Locate every blood parasite and identify its species.
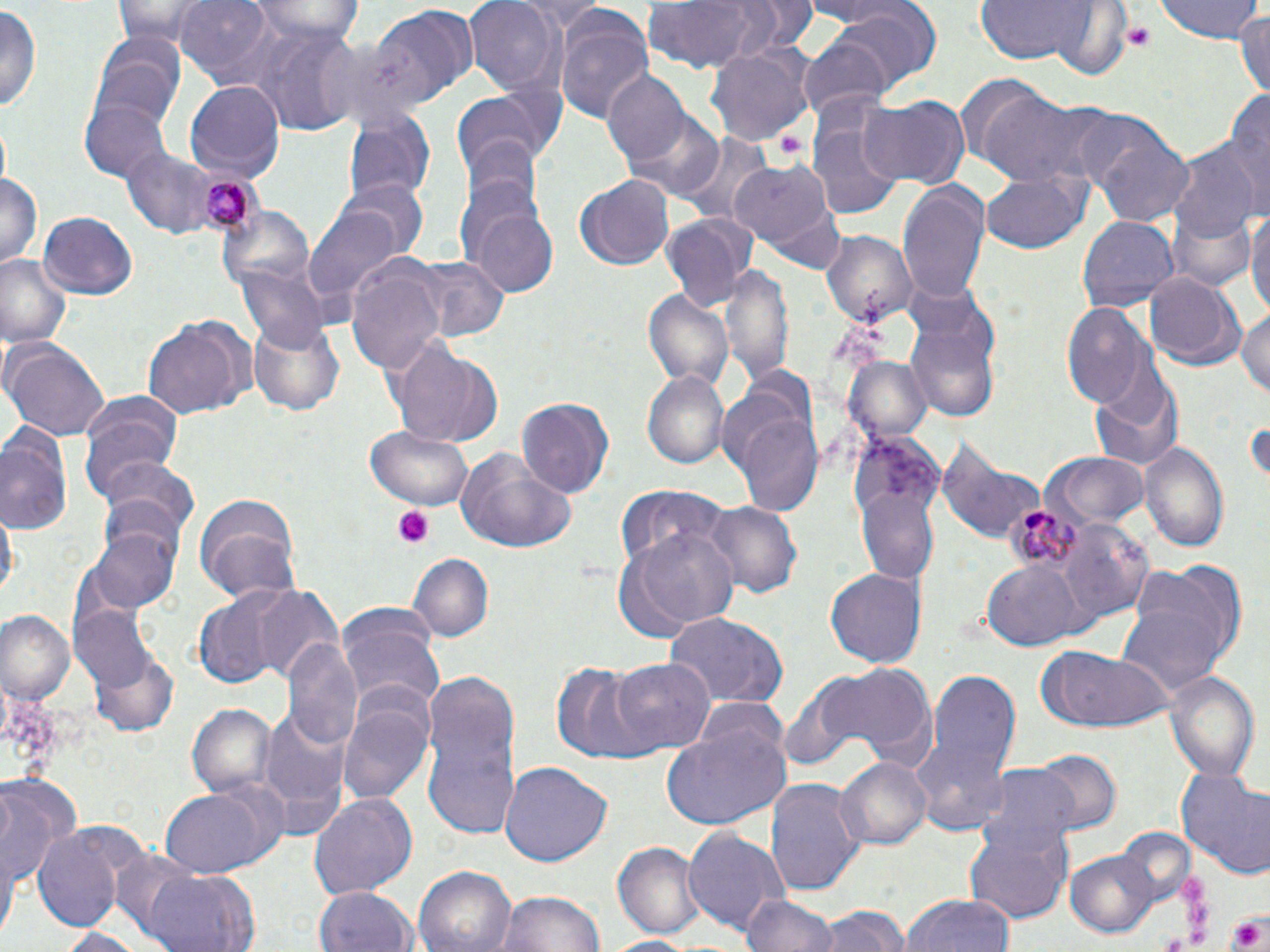

Approximate bounding boxes as named x1/y1/x2/y2 corners in pixels.
Plasmodium malariae-infected red blood cells: (x1=196, y1=168, x2=269, y2=239), (x1=997, y1=501, x2=1089, y2=581).
No Plasmodium falciparum, Plasmodium ovale, Plasmodium vivax, Babesia divergens, or Trypanosoma brucei observed.

{
  "slide_level_diagnosis": "Plasmodium malariae",
  "image_size": "1270×952 pixels",
  "field_of_view": "one of a larger specimen",
  "modality": "light microscopy",
  "stain": "May-Grünwald-Giemsa",
  "preparation": "thin blood film",
  "magnification": "1000x",
  "uninfected_red_blood_cell_locations": "approximate bounding boxes as named x1/y1/x2/y2 corners in pixels: (x1=107, y1=0, x2=236, y2=46), (x1=172, y1=0, x2=283, y2=88), (x1=253, y1=0, x2=365, y2=49), (x1=465, y1=0, x2=563, y2=94), (x1=514, y1=0, x2=610, y2=27), (x1=644, y1=0, x2=774, y2=75), (x1=818, y1=0, x2=944, y2=85), (x1=972, y1=0, x2=1109, y2=65), (x1=1154, y1=0, x2=1264, y2=43), (x1=1046, y1=2, x2=1134, y2=79), (x1=550, y1=4, x2=655, y2=126), (x1=361, y1=5, x2=479, y2=109), (x1=0, y1=6, x2=42, y2=116), (x1=1234, y1=11, x2=1270, y2=96), (x1=243, y1=25, x2=364, y2=132), (x1=797, y1=35, x2=897, y2=117), (x1=707, y1=41, x2=815, y2=148), (x1=90, y1=48, x2=184, y2=134), (x1=600, y1=72, x2=692, y2=169), (x1=955, y1=74, x2=1057, y2=172), (x1=186, y1=82, x2=285, y2=181), (x1=971, y1=85, x2=1105, y2=190), (x1=1224, y1=85, x2=1269, y2=220), (x1=452, y1=92, x2=552, y2=178), (x1=860, y1=95, x2=971, y2=188), (x1=82, y1=97, x2=171, y2=183), (x1=806, y1=105, x2=907, y2=222), (x1=342, y1=109, x2=434, y2=203), (x1=624, y1=110, x2=726, y2=201), (x1=1068, y1=111, x2=1172, y2=197), (x1=675, y1=132, x2=774, y2=226), (x1=1094, y1=134, x2=1197, y2=226), (x1=459, y1=136, x2=544, y2=222), (x1=1169, y1=145, x2=1258, y2=247), (x1=117, y1=146, x2=230, y2=240), (x1=455, y1=150, x2=552, y2=277), (x1=729, y1=159, x2=842, y2=264), (x1=0, y1=169, x2=42, y2=271), (x1=981, y1=173, x2=1091, y2=254), (x1=574, y1=175, x2=674, y2=271), (x1=343, y1=179, x2=430, y2=261), (x1=897, y1=180, x2=990, y2=302), (x1=465, y1=202, x2=560, y2=300), (x1=215, y1=204, x2=317, y2=297), (x1=1246, y1=204, x2=1270, y2=325), (x1=303, y1=207, x2=404, y2=312), (x1=663, y1=211, x2=759, y2=312), (x1=1168, y1=211, x2=1256, y2=293), (x1=39, y1=212, x2=138, y2=299), (x1=1077, y1=216, x2=1179, y2=312), (x1=822, y1=230, x2=915, y2=327), (x1=0, y1=255, x2=71, y2=349), (x1=401, y1=255, x2=509, y2=344), (x1=346, y1=256, x2=448, y2=373), (x1=234, y1=264, x2=327, y2=351), (x1=722, y1=265, x2=792, y2=384), (x1=1144, y1=273, x2=1243, y2=370), (x1=643, y1=291, x2=733, y2=392), (x1=1237, y1=304, x2=1270, y2=404), (x1=1061, y1=305, x2=1151, y2=410), (x1=247, y1=317, x2=343, y2=418), (x1=143, y1=318, x2=244, y2=421), (x1=906, y1=320, x2=1002, y2=425), (x1=4, y1=338, x2=111, y2=444), (x1=386, y1=341, x2=505, y2=448), (x1=843, y1=355, x2=933, y2=445), (x1=1089, y1=371, x2=1184, y2=473), (x1=643, y1=372, x2=731, y2=472), (x1=80, y1=393, x2=181, y2=501), (x1=517, y1=396, x2=615, y2=500), (x1=725, y1=396, x2=826, y2=517), (x1=0, y1=423, x2=75, y2=538), (x1=364, y1=424, x2=476, y2=509), (x1=848, y1=431, x2=946, y2=584), (x1=936, y1=438, x2=1041, y2=546), (x1=1139, y1=443, x2=1230, y2=555), (x1=456, y1=449, x2=577, y2=555), (x1=1051, y1=452, x2=1150, y2=526), (x1=100, y1=456, x2=201, y2=542), (x1=615, y1=487, x2=733, y2=585), (x1=191, y1=490, x2=303, y2=605), (x1=702, y1=500, x2=802, y2=600), (x1=1055, y1=515, x2=1153, y2=623), (x1=90, y1=525, x2=180, y2=613), (x1=630, y1=525, x2=744, y2=633), (x1=408, y1=553, x2=494, y2=642), (x1=1117, y1=559, x2=1239, y2=701), (x1=980, y1=561, x2=1087, y2=651), (x1=826, y1=569, x2=926, y2=667), (x1=244, y1=585, x2=343, y2=678), (x1=194, y1=591, x2=289, y2=687), (x1=75, y1=606, x2=154, y2=691), (x1=0, y1=611, x2=74, y2=706), (x1=663, y1=611, x2=789, y2=708), (x1=338, y1=615, x2=444, y2=708), (x1=284, y1=639, x2=364, y2=754), (x1=90, y1=646, x2=181, y2=738), (x1=1037, y1=646, x2=1174, y2=731), (x1=609, y1=658, x2=713, y2=755), (x1=550, y1=662, x2=653, y2=762), (x1=791, y1=662, x2=942, y2=772), (x1=421, y1=664, x2=524, y2=845), (x1=910, y1=667, x2=1022, y2=834), (x1=1166, y1=672, x2=1259, y2=784), (x1=338, y1=689, x2=436, y2=806), (x1=187, y1=704, x2=277, y2=799), (x1=259, y1=705, x2=352, y2=832), (x1=662, y1=723, x2=790, y2=831), (x1=1028, y1=749, x2=1125, y2=833), (x1=835, y1=756, x2=932, y2=852), (x1=501, y1=761, x2=613, y2=867), (x1=1175, y1=766, x2=1270, y2=876), (x1=974, y1=767, x2=1083, y2=852), (x1=0, y1=776, x2=80, y2=894), (x1=766, y1=778, x2=865, y2=900), (x1=159, y1=781, x2=287, y2=879), (x1=310, y1=792, x2=417, y2=901), (x1=965, y1=819, x2=1074, y2=922), (x1=34, y1=826, x2=127, y2=934), (x1=684, y1=828, x2=788, y2=937), (x1=613, y1=841, x2=703, y2=937), (x1=1065, y1=850, x2=1165, y2=940), (x1=127, y1=861, x2=264, y2=952), (x1=416, y1=867, x2=514, y2=952), (x1=315, y1=885, x2=418, y2=952), (x1=498, y1=889, x2=609, y2=952), (x1=738, y1=893, x2=836, y2=952), (x1=903, y1=894, x2=1016, y2=952), (x1=811, y1=906, x2=915, y2=952), (x1=52, y1=926, x2=155, y2=951), (x1=601, y1=936, x2=700, y2=952)",
  "platelet_locations": "approximate bounding boxes as named x1/y1/x2/y2 corners in pixels: (x1=1122, y1=24, x2=1155, y2=48), (x1=394, y1=506, x2=436, y2=549), (x1=1176, y1=872, x2=1207, y2=903), (x1=1183, y1=900, x2=1210, y2=927), (x1=1227, y1=911, x2=1270, y2=952), (x1=1186, y1=926, x2=1212, y2=944)"
}